Comment on the morphology of the red blood cells.
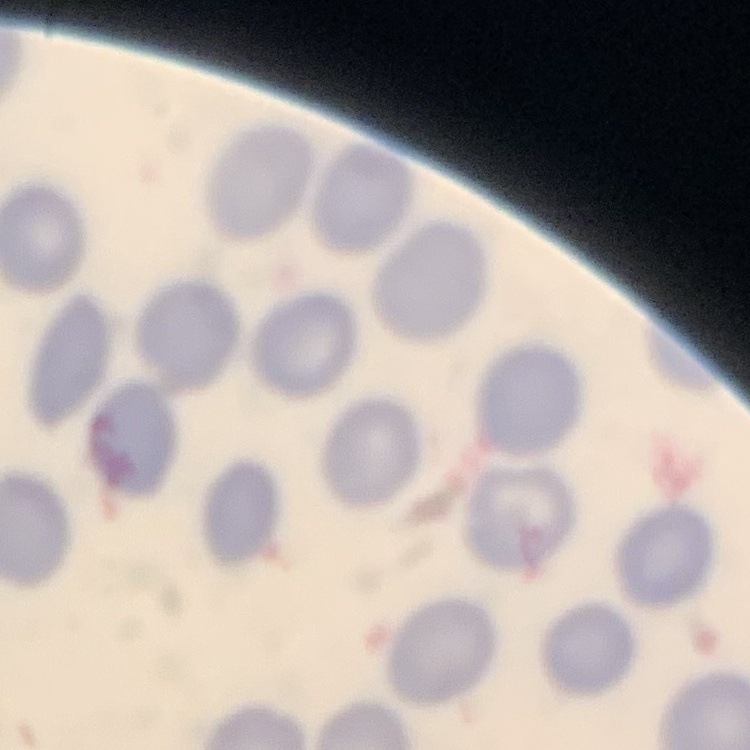
They show no rouleaux formation.

Summary:
  - Image type: square crop of a larger photomicrograph
  - Preparation: thin blood film
  - Stain: Field's or Giemsa